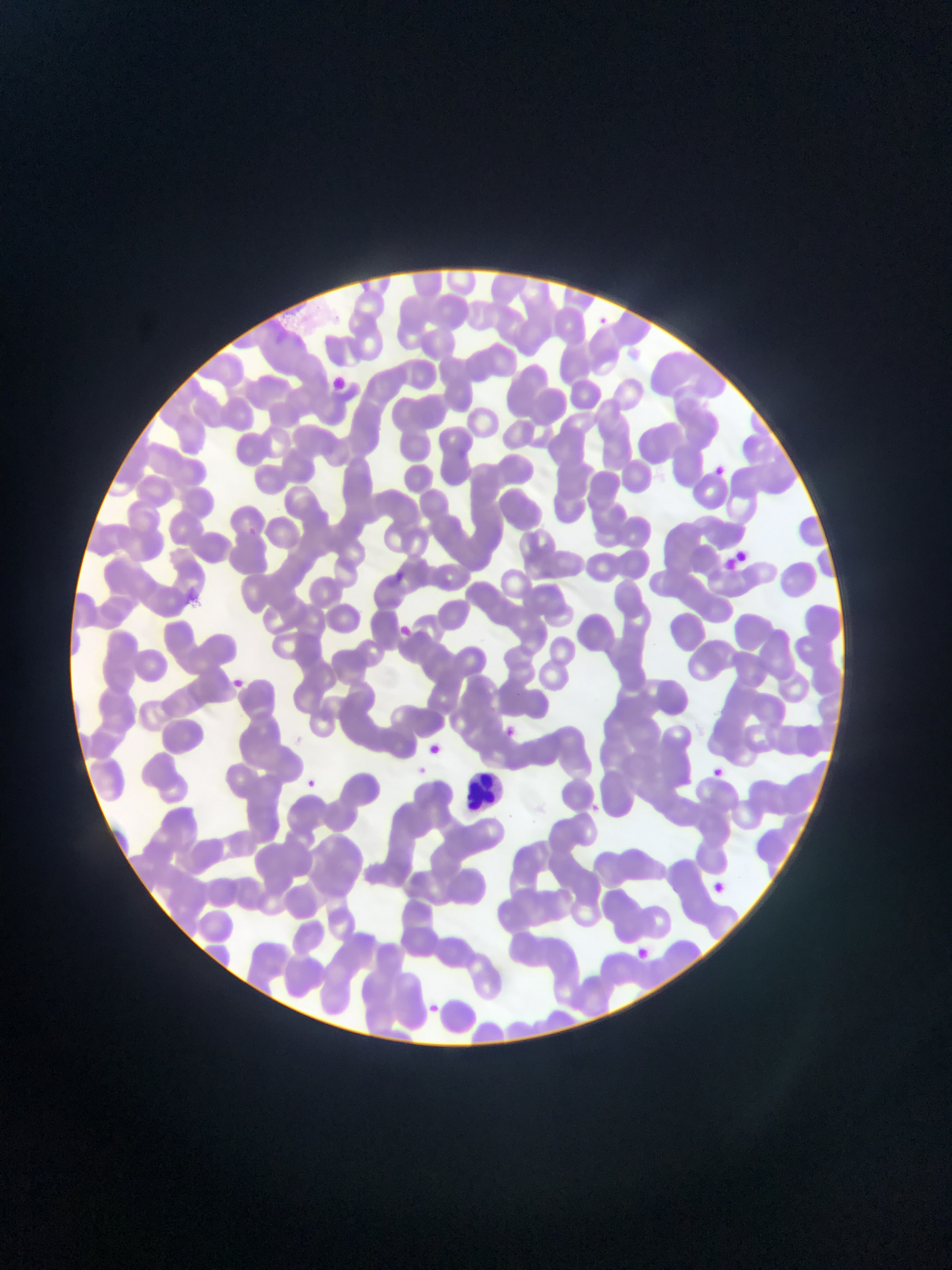
Approximate bounding boxes as [left, top, right, bottom] in pixels. Malaria parasite locations: [601, 308, 611, 330], [717, 461, 735, 482], [244, 523, 268, 545], [392, 570, 408, 583], [401, 620, 420, 640], [236, 676, 251, 691], [501, 723, 520, 735], [428, 742, 446, 763], [711, 761, 734, 781], [304, 775, 322, 796], [427, 998, 448, 1014]. Leukocyte locations: [455, 762, 508, 813]. Image is 952×1270 pixels. Mobile-phone photograph taken through the microscope. One field of view. Collected in Ghana. Thin blood smear.